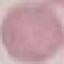
Summary:
  - Malaria status: uninfected
  - Capture: smartphone camera at the microscope eyepiece
  - Stain: Giemsa
  - Preparation: thin blood smear
  - Image type: automatically extracted cell patch, resized to 64 × 64 pixels